State which cell type is depicted.
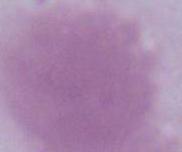

An erythrocyte.

Summary:
  - Modality: photomicrograph
  - Magnification: 1000x